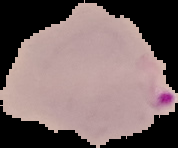
From a thin blood smear. Result: malaria parasites detected. Segmented cell region on a black background. Image is 178×148 pixels.